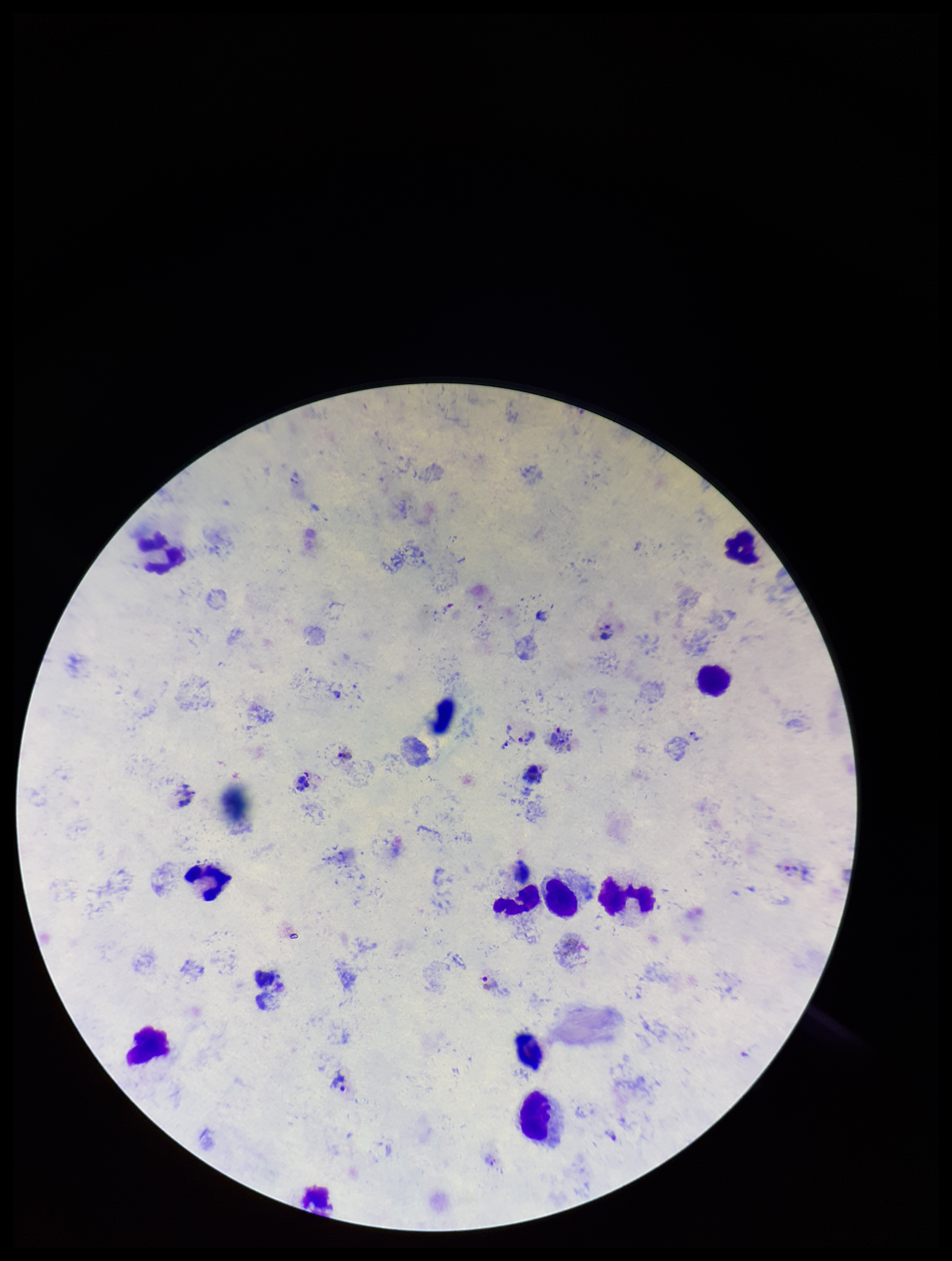

field of view = single
patient malaria status = infected
species reported for this patient = Plasmodium vivax
leukocyte count = 13
capture = smartphone photograph through the microscope eyepiece
image size = 952×1261 pixels
parasite count = 3
stain = Giemsa
preparation = thick smear
Plasmodium parasites = detected